Point out leukocytes.
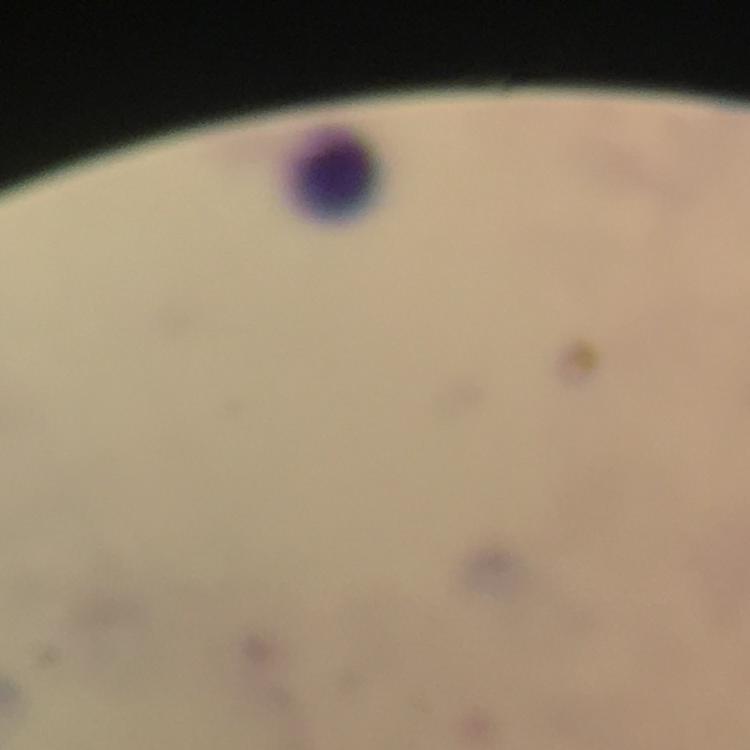
Approximate centers as (x, y) in pixels.
Leukocytes: (337, 169).

magnification = 100x
image size = 750×750 pixels
preparation = thick smear
immersion oil = applied
context = from a diagnostic examination for malaria
capture = smartphone camera through the microscope
stain = Giemsa
malaria parasites = none seen
cropped from = a single field of view